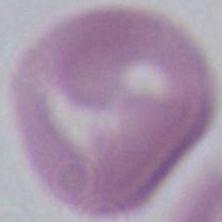
{
  "identification": "red blood cell",
  "modality": "micrograph",
  "magnification": "1000x"
}